Describe the morphology of the erythrocytes.
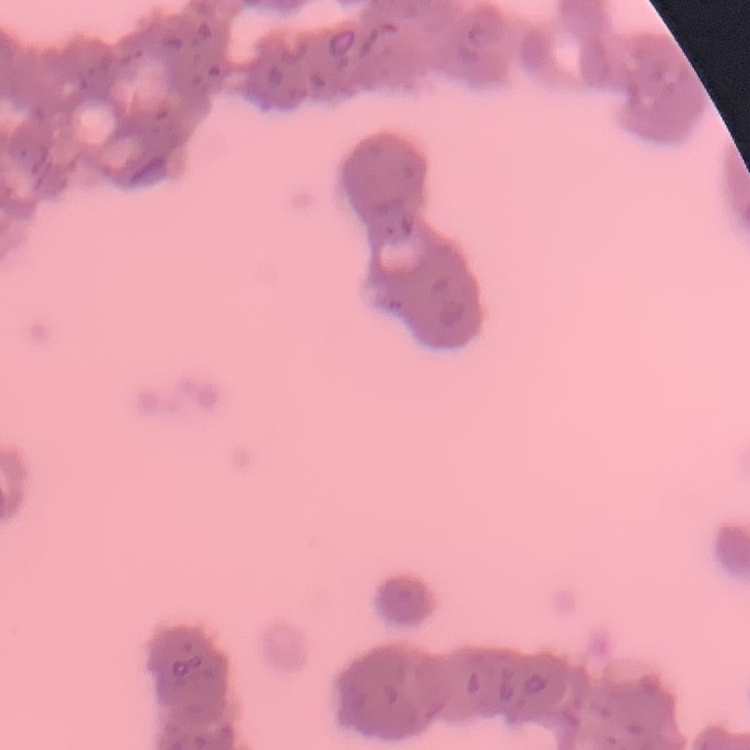
They show rouleaux formation.

{
  "image_type": "square crop of a larger photomicrograph",
  "stain": "Field's or Giemsa",
  "preparation": "thin blood film"
}